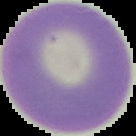 Result: no malaria parasites seen. The area outside the segmented cell region is set to black. Image is 136×136 pixels. From a thin blood smear.